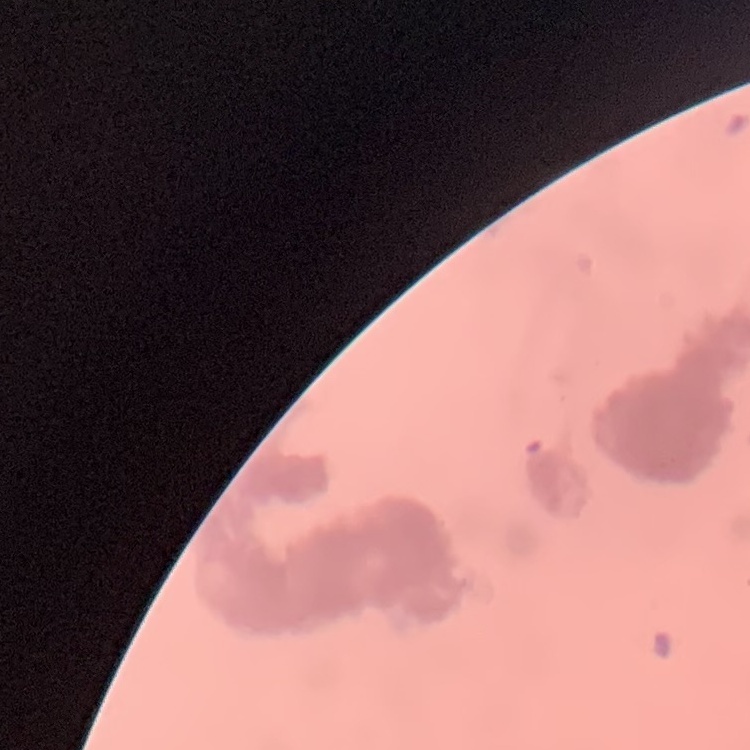
{
  "erythrocyte_morphology": "rouleaux formation",
  "preparation": "thin blood film",
  "image_type": "one tile cut from a larger photomicrograph",
  "stain": "Field's or Giemsa"
}